State the preparation type.
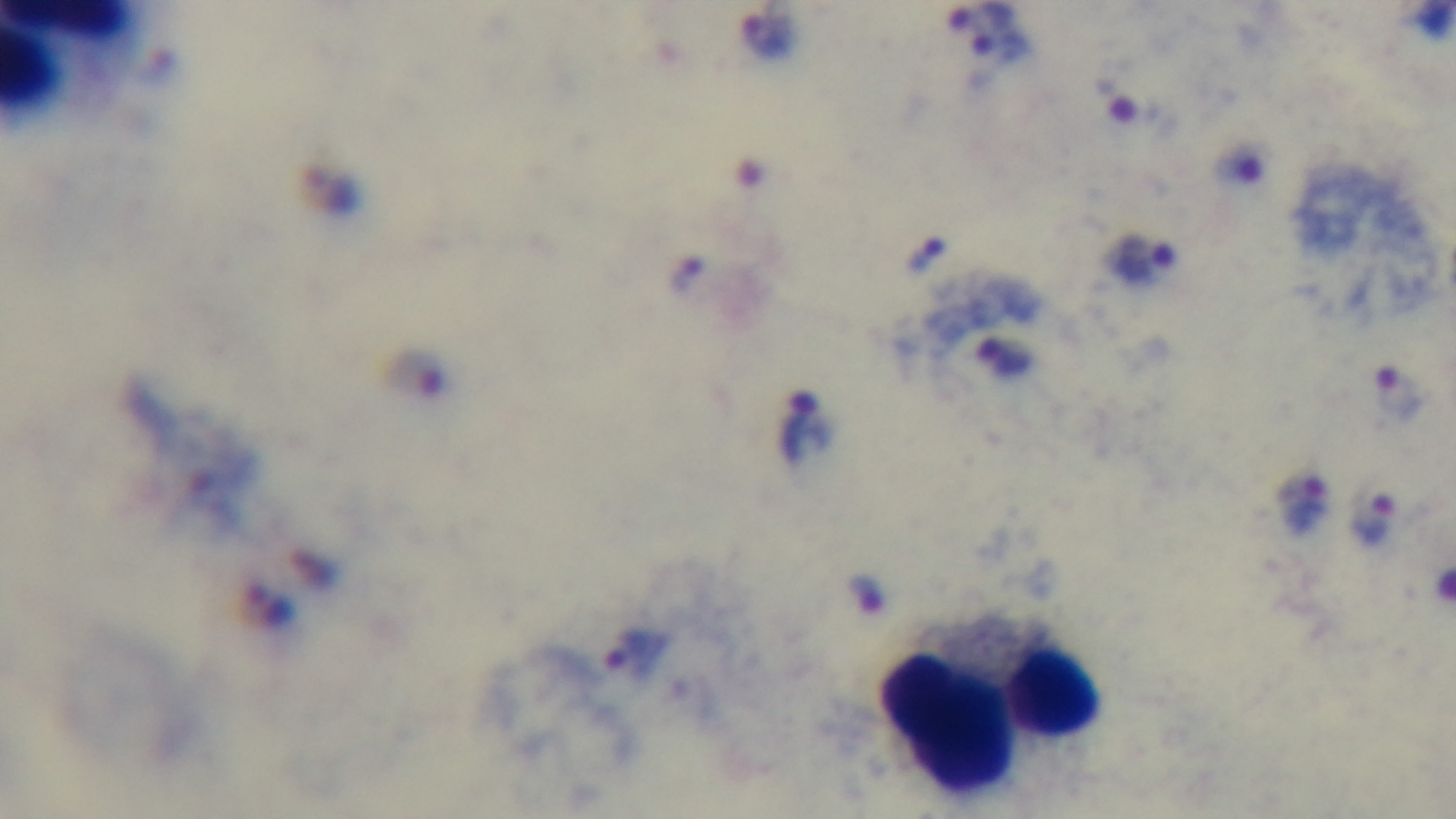
It is a thick blood film.

stain = Giemsa
capture = mounted 4K digital camera
modality = light microscopy
malaria status = infected
field of view = one from the slide
objective = 100x oil immersion